Assess the morphology of the erythrocytes.
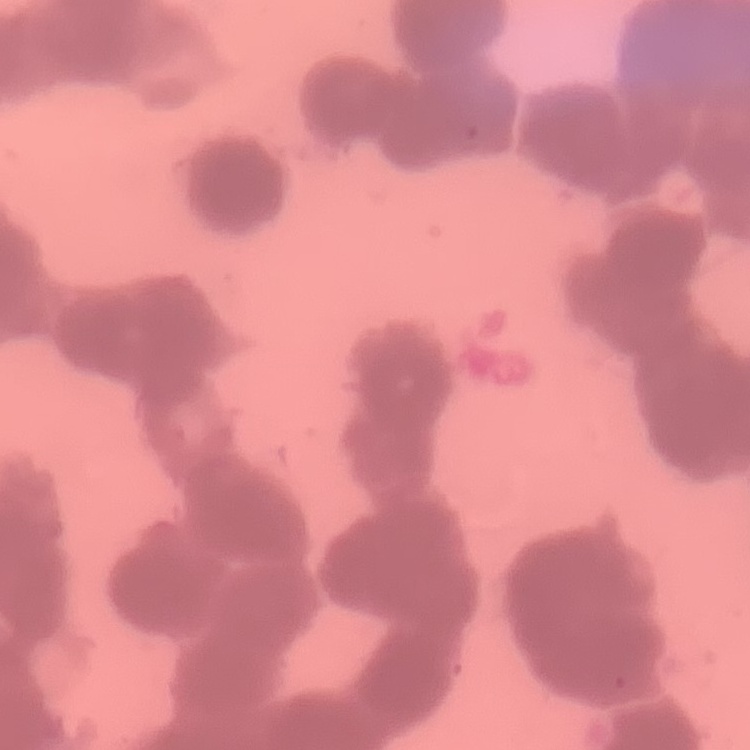
Rouleaux formation.

Field's or Giemsa stain. Thin blood smear. Square crop of a larger photomicrograph.